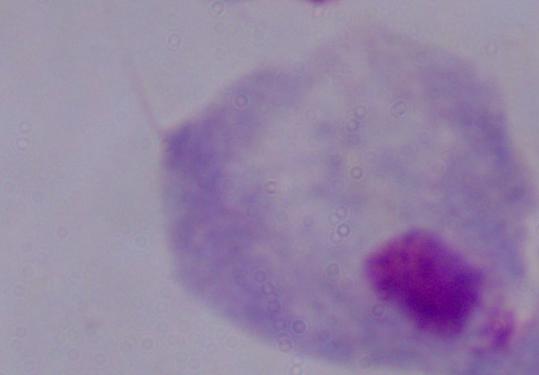

Summary:
  - Modality: photomicrograph
  - Magnification: 1000x
  - Identification: trichomonad